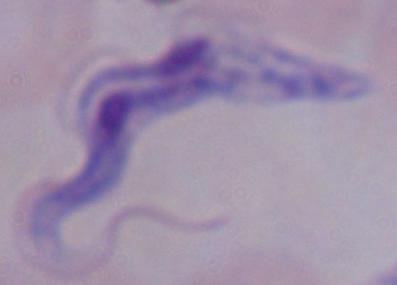
Summary:
  - Modality: micrograph
  - Magnification: 1000x
  - Identification: trypanosome